Report the malaria status of this cell.
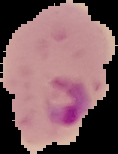

Parasitized.

Summary:
  - Image size: 118×154 pixels
  - Preparation: thin blood film
  - Image type: cell region segmented out of the field of view; surrounding area masked to black